Locate every Trypanosoma brucei.
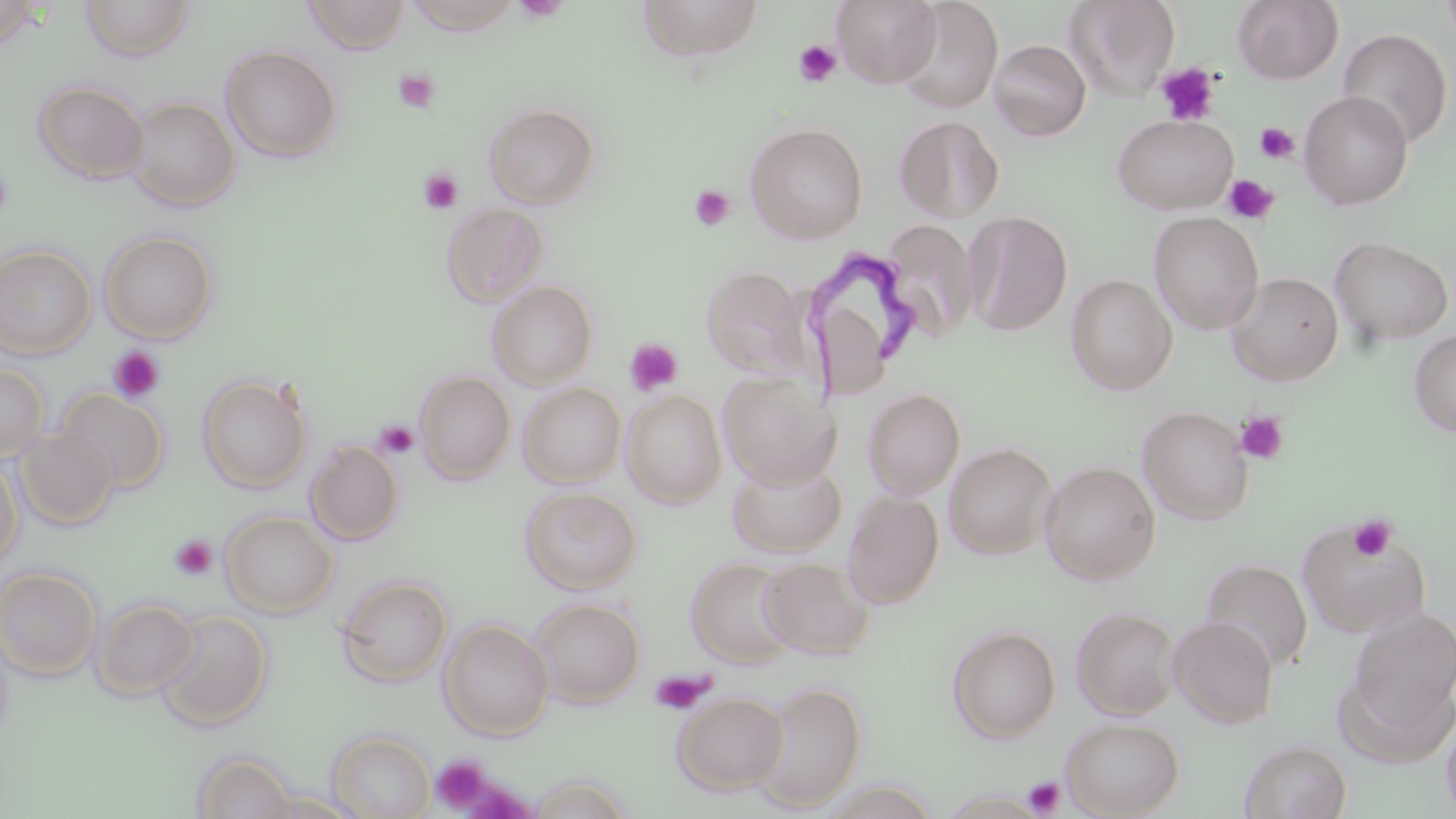
Approximate bounding boxes as (x1,y1)-(x2,y2) corner pairs in pixels.
Trypanosoma brucei: (804,249)-(916,398).

Summary:
  - Platelet locations: (793,40)-(842,87), (1156,62)-(1220,125), (394,70)-(439,113), (1255,122)-(1299,164), (0,167)-(15,218), (418,168)-(464,215), (1222,174)-(1279,224), (689,185)-(736,231), (624,338)-(683,397), (107,345)-(166,404), (1235,411)-(1288,463), (373,421)-(419,459), (1348,515)-(1397,562), (169,534)-(218,581), (650,670)-(713,715), (431,755)-(493,811), (1023,776)-(1065,817)
  - Uninfected red blood cell locations: (0,0)-(42,52), (80,0)-(195,62), (301,0)-(410,54), (636,0)-(767,62), (832,0)-(942,88), (895,0)-(1003,114), (1064,0)-(1181,100), (1232,0)-(1343,85), (405,1)-(520,34), (1439,1)-(1456,49), (1338,27)-(1453,150), (989,39)-(1091,141), (220,45)-(342,163), (32,80)-(149,185), (1299,91)-(1413,210), (124,97)-(240,211), (483,102)-(599,208), (1112,114)-(1238,215), (895,116)-(1004,222), (745,122)-(868,243), (440,202)-(548,307), (964,211)-(1072,336), (1149,212)-(1265,335), (880,220)-(981,344), (99,230)-(218,343), (1329,236)-(1454,347), (0,244)-(97,361), (701,265)-(815,379), (1226,272)-(1343,386), (1066,274)-(1178,394), (487,280)-(597,389), (1410,329)-(1456,437), (0,363)-(49,463), (414,371)-(515,485), (718,371)-(839,488), (196,374)-(312,494), (517,382)-(626,487), (57,387)-(170,492), (862,388)-(965,499), (621,391)-(727,509), (1137,406)-(1255,525), (14,424)-(120,530), (305,440)-(403,545), (944,443)-(1057,560), (0,456)-(24,569), (727,458)-(846,558), (1039,461)-(1160,584), (519,486)-(641,595), (842,490)-(944,609), (220,510)-(339,618), (1296,519)-(1429,639), (685,556)-(800,669), (758,557)-(874,659), (1201,559)-(1312,672), (0,566)-(103,682), (335,575)-(452,688), (89,596)-(201,702), (527,598)-(646,708), (1071,606)-(1181,719), (1347,606)-(1456,734), (155,610)-(272,731), (1168,616)-(1278,728), (438,619)-(554,740), (947,625)-(1061,743), (748,682)-(866,812), (672,692)-(790,796), (1440,713)-(1456,819), (1061,718)-(1184,818), (326,729)-(436,819), (1239,739)-(1351,819), (191,750)-(297,818), (528,776)-(634,819), (255,790)-(365,818)
  - Slide-level diagnosis: Trypanosoma brucei
  - Magnification: 1000x
  - Field of view: single
  - Image size: 1456×819 pixels
  - Stain: May-Grünwald-Giemsa
  - Preparation: thin blood film
  - Modality: light microscopy